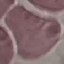

malaria status = uninfected
preparation = thin blood film
capture = smartphone through the microscope eyepiece
stain = Giemsa
image type = cell patch, automatically extracted from a larger field of view and resized to 64 × 64 pixels